Classify this cell by malaria status.
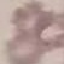

It is uninfected.

capture = smartphone through the microscope eyepiece
image type = cell patch, automatically extracted from a larger field of view and resized to 64 × 64 pixels
preparation = thin smear
stain = Giemsa